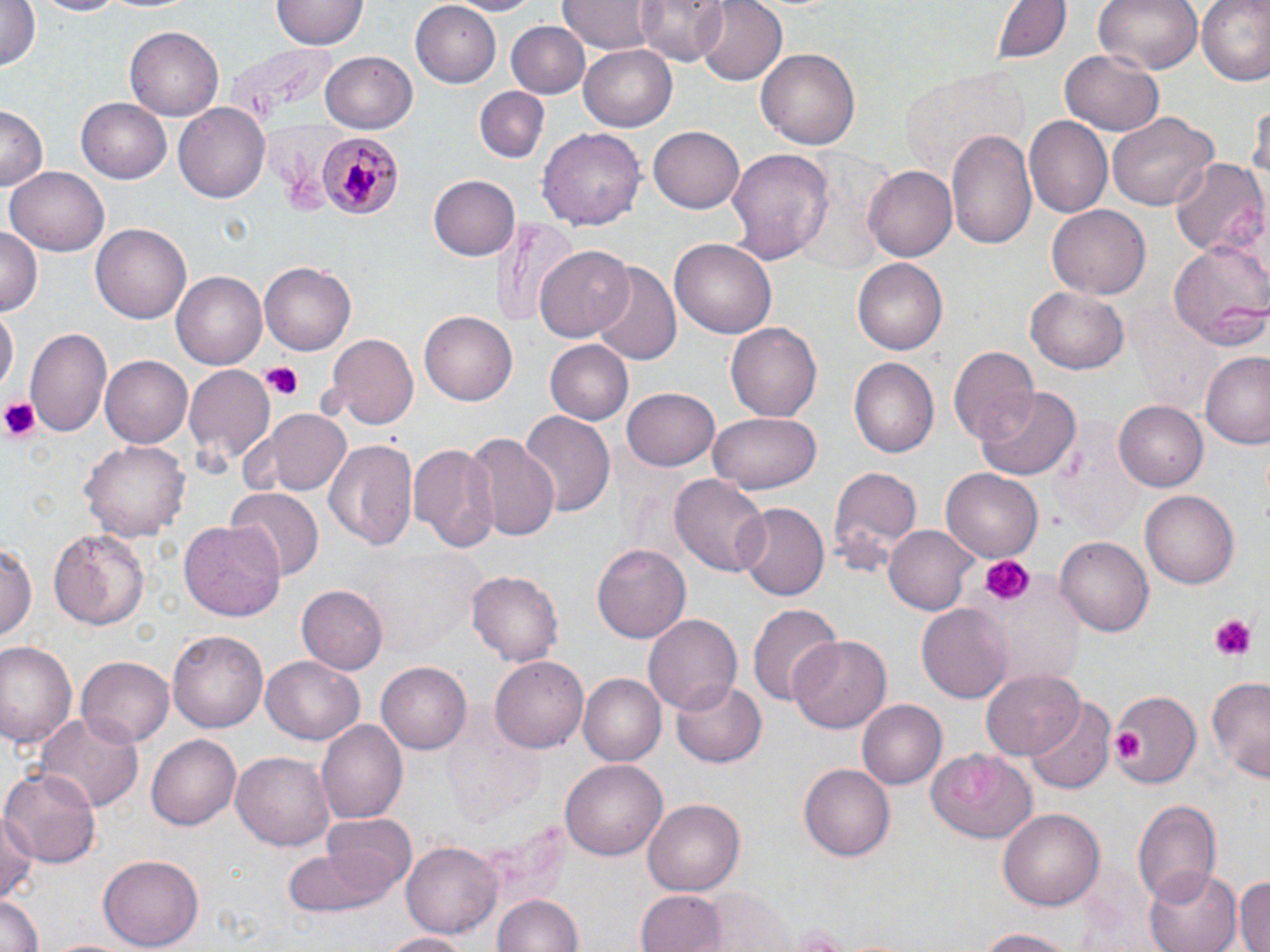

Summary:
  - Coordinate format: approximate bounding boxes as named x1/y1/x2/y2 corners in pixels
  - Platelet locations: (x1=259, y1=361, x2=303, y2=397), (x1=0, y1=397, x2=38, y2=442), (x1=981, y1=556, x2=1034, y2=607), (x1=1208, y1=614, x2=1259, y2=662), (x1=1110, y1=730, x2=1144, y2=765)
  - Uninfected red blood cell locations: (x1=0, y1=0, x2=43, y2=74), (x1=34, y1=0, x2=125, y2=17), (x1=448, y1=0, x2=543, y2=15), (x1=557, y1=0, x2=655, y2=53), (x1=637, y1=0, x2=729, y2=64), (x1=692, y1=0, x2=786, y2=85), (x1=990, y1=0, x2=1073, y2=65), (x1=1092, y1=0, x2=1202, y2=74), (x1=1197, y1=0, x2=1270, y2=86), (x1=270, y1=2, x2=366, y2=51), (x1=410, y1=2, x2=502, y2=87), (x1=505, y1=20, x2=590, y2=99), (x1=126, y1=25, x2=225, y2=119), (x1=579, y1=43, x2=678, y2=130), (x1=1060, y1=48, x2=1166, y2=136), (x1=757, y1=49, x2=862, y2=151), (x1=320, y1=51, x2=418, y2=134), (x1=901, y1=67, x2=1024, y2=173), (x1=475, y1=84, x2=551, y2=161), (x1=1250, y1=94, x2=1270, y2=196), (x1=76, y1=98, x2=172, y2=182), (x1=174, y1=102, x2=272, y2=201), (x1=1, y1=106, x2=48, y2=192), (x1=1108, y1=111, x2=1218, y2=211), (x1=1025, y1=116, x2=1113, y2=220), (x1=649, y1=126, x2=747, y2=213), (x1=537, y1=127, x2=644, y2=230), (x1=946, y1=129, x2=1038, y2=252), (x1=728, y1=147, x2=834, y2=265), (x1=1170, y1=158, x2=1266, y2=257), (x1=863, y1=165, x2=956, y2=262), (x1=5, y1=167, x2=108, y2=257), (x1=428, y1=175, x2=519, y2=261), (x1=1049, y1=205, x2=1149, y2=298), (x1=489, y1=218, x2=579, y2=329), (x1=93, y1=223, x2=192, y2=324), (x1=0, y1=224, x2=43, y2=314), (x1=670, y1=235, x2=777, y2=335), (x1=1168, y1=239, x2=1269, y2=348), (x1=536, y1=244, x2=636, y2=342), (x1=852, y1=259, x2=945, y2=355), (x1=586, y1=260, x2=685, y2=365), (x1=259, y1=262, x2=356, y2=355), (x1=171, y1=271, x2=269, y2=369), (x1=1027, y1=287, x2=1130, y2=374), (x1=0, y1=304, x2=17, y2=396), (x1=420, y1=311, x2=517, y2=405), (x1=726, y1=322, x2=822, y2=422), (x1=26, y1=327, x2=112, y2=437), (x1=323, y1=333, x2=418, y2=429), (x1=546, y1=339, x2=635, y2=425), (x1=948, y1=346, x2=1038, y2=447), (x1=1199, y1=351, x2=1270, y2=449), (x1=101, y1=357, x2=192, y2=449), (x1=849, y1=358, x2=939, y2=458), (x1=184, y1=365, x2=274, y2=463), (x1=623, y1=387, x2=719, y2=471), (x1=976, y1=388, x2=1080, y2=480), (x1=1116, y1=401, x2=1209, y2=490), (x1=254, y1=408, x2=352, y2=497), (x1=519, y1=411, x2=615, y2=519), (x1=710, y1=412, x2=820, y2=494), (x1=466, y1=432, x2=562, y2=544), (x1=81, y1=438, x2=188, y2=542), (x1=325, y1=439, x2=419, y2=550), (x1=409, y1=443, x2=500, y2=553), (x1=827, y1=464, x2=923, y2=578), (x1=941, y1=469, x2=1042, y2=563), (x1=670, y1=474, x2=768, y2=576), (x1=226, y1=486, x2=324, y2=582), (x1=1140, y1=491, x2=1241, y2=590), (x1=733, y1=501, x2=829, y2=603), (x1=180, y1=518, x2=287, y2=625), (x1=883, y1=523, x2=977, y2=615), (x1=49, y1=525, x2=152, y2=632), (x1=1055, y1=534, x2=1152, y2=633), (x1=0, y1=538, x2=37, y2=647), (x1=592, y1=544, x2=690, y2=643), (x1=364, y1=550, x2=482, y2=655), (x1=466, y1=567, x2=564, y2=664), (x1=296, y1=585, x2=387, y2=674), (x1=746, y1=602, x2=841, y2=707), (x1=917, y1=603, x2=1013, y2=703), (x1=644, y1=613, x2=741, y2=716), (x1=167, y1=631, x2=267, y2=733), (x1=788, y1=636, x2=892, y2=733), (x1=0, y1=642, x2=78, y2=750), (x1=261, y1=654, x2=364, y2=744), (x1=77, y1=655, x2=175, y2=749), (x1=491, y1=655, x2=592, y2=753), (x1=376, y1=662, x2=471, y2=755), (x1=980, y1=668, x2=1086, y2=757), (x1=1207, y1=673, x2=1270, y2=785), (x1=580, y1=675, x2=664, y2=767), (x1=672, y1=677, x2=764, y2=768), (x1=1105, y1=687, x2=1200, y2=791), (x1=1026, y1=696, x2=1116, y2=794), (x1=856, y1=700, x2=945, y2=789), (x1=32, y1=712, x2=145, y2=816), (x1=316, y1=720, x2=408, y2=826), (x1=147, y1=734, x2=241, y2=831), (x1=926, y1=747, x2=1037, y2=845), (x1=233, y1=750, x2=337, y2=851), (x1=559, y1=755, x2=666, y2=859), (x1=800, y1=763, x2=895, y2=861), (x1=1, y1=765, x2=100, y2=868), (x1=642, y1=798, x2=744, y2=894), (x1=1132, y1=798, x2=1222, y2=903), (x1=999, y1=807, x2=1105, y2=909), (x1=321, y1=812, x2=417, y2=895), (x1=1, y1=813, x2=37, y2=903), (x1=402, y1=840, x2=502, y2=937), (x1=282, y1=844, x2=395, y2=918), (x1=99, y1=855, x2=202, y2=950), (x1=1146, y1=865, x2=1241, y2=952), (x1=1234, y1=875, x2=1270, y2=952), (x1=698, y1=888, x2=800, y2=952), (x1=636, y1=891, x2=725, y2=952), (x1=492, y1=892, x2=582, y2=952), (x1=0, y1=895, x2=45, y2=952), (x1=786, y1=920, x2=857, y2=949), (x1=971, y1=926, x2=1083, y2=950), (x1=378, y1=931, x2=471, y2=952)
  - Plasmodium malariae-infected red blood cell locations: (x1=313, y1=130, x2=404, y2=220)
  - Slide-level diagnosis: Plasmodium malariae
  - Modality: optical microscopy
  - Preparation: thin blood smear
  - Field of view: one of a larger specimen
  - Image size: 1270×952 pixels
  - Magnification: 1000x
  - Stain: May-Grünwald-Giemsa